Assess this cell for malaria.
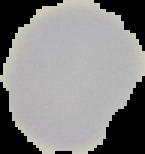

It is uninfected.

image_type: cell region segmented out of the field of view; surrounding area masked to black
image_size: 145×154 pixels
preparation: thin blood film